Outline every trophozoite.
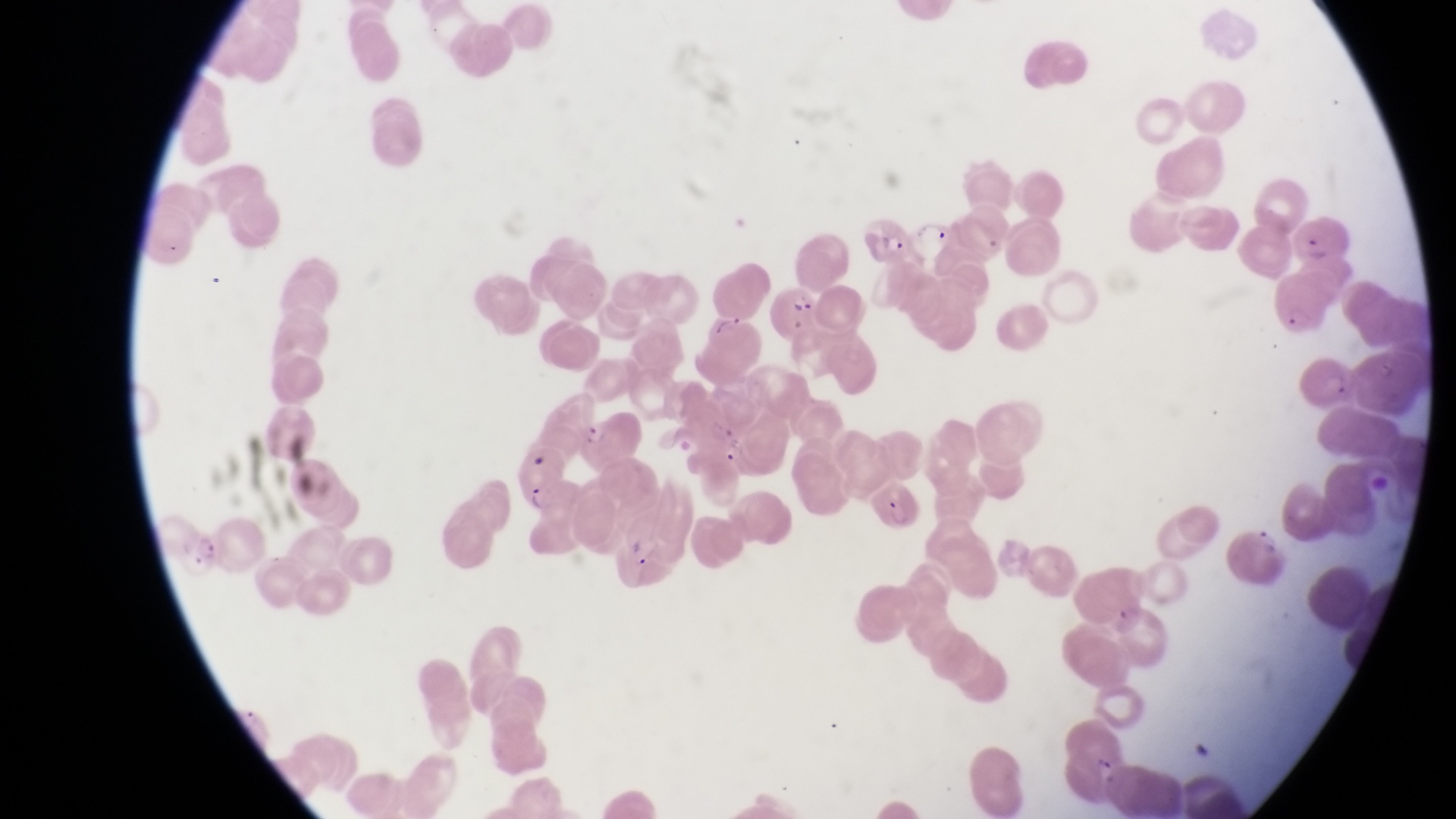

Approximate bounding boxes as left top right bottom in pixels.
Trophozoites: 914 217 948 247.

field of view = single
magnification = 1000x
parasitised red blood cell locations = approximate bounding boxes as left top right bottom in pixels: 858 211 908 260; 1277 272 1330 341; 1304 356 1363 415; 579 417 629 469; 516 465 563 514; 869 482 922 538; 153 510 222 581
image size = 1456×819 pixels
country = Uganda
artifact (platelet-like body, stain precipitate, or debris) locations = approximate bounding boxes as left top right bottom in pixels: 769 285 825 330
capture = smartphone photograph through the eyepiece of an Olympus CX-23 microscope
preparation = thin blood smear